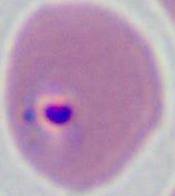

Summary:
  - Identification: Plasmodium
  - Magnification: 400x or 1000x
  - Modality: photomicrograph